Report the malaria status of this cell.
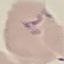

It is parasitized.

preparation = thin blood film
capture = smartphone camera at the microscope eyepiece
stain = Giemsa
image type = automatically extracted cell patch, resized to 64 × 64 pixels